State which parasite is depicted.
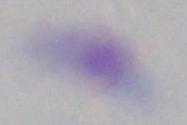

This is Toxoplasma gondii.

Captured at 1000x magnification. Micrograph.